Locate every Plasmodium parasite and every leukocyte.
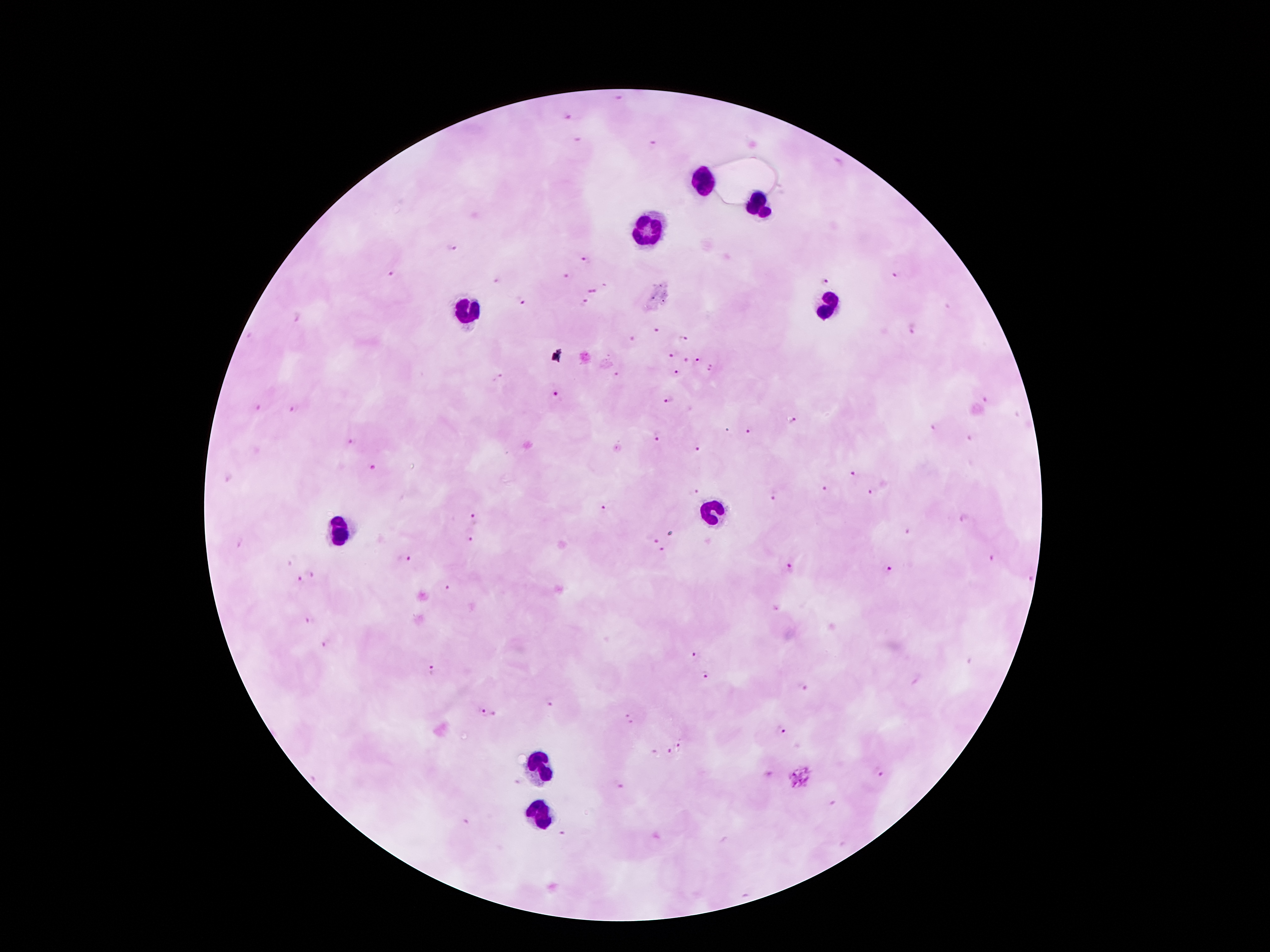

Approximate centers as (x, y) in pixels.
Plasmodium parasites: (619, 97), (568, 116), (652, 145), (451, 248), (586, 261), (392, 275), (568, 275), (898, 275), (825, 281), (605, 285), (592, 291), (520, 300), (585, 301), (295, 318), (911, 328), (656, 330), (684, 338), (631, 339), (670, 353), (687, 359), (697, 359), (711, 368), (617, 372), (677, 373), (497, 378), (555, 394), (668, 400), (985, 401), (258, 409), (292, 409), (792, 422), (936, 428), (749, 430), (657, 437), (969, 440), (350, 442), (696, 449), (373, 467), (856, 475), (227, 479), (827, 488), (698, 490), (873, 491), (775, 493), (602, 509), (473, 516), (964, 519), (470, 540), (652, 540), (240, 542), (661, 551), (989, 559), (406, 561), (789, 569), (890, 571), (311, 575), (1027, 578), (299, 581), (448, 588), (310, 620), (327, 644), (695, 655), (431, 671), (705, 675), (803, 686), (548, 706), (479, 712), (494, 716), (629, 722), (782, 729), (679, 747), (655, 752), (670, 753), (877, 772), (766, 774), (801, 777), (620, 786), (830, 803), (467, 822), (561, 833).
Leukocytes: (702, 183), (759, 207), (651, 227), (471, 305), (829, 308), (715, 512), (341, 533), (539, 767), (542, 815).

magnification = 100x
stain = Giemsa
capture = smartphone camera through the microscope eyepiece
preparation = thick peripheral-blood smear
field of view = one from this slide
patient malaria status = infected with Plasmodium falciparum
image size = 1270×952 pixels